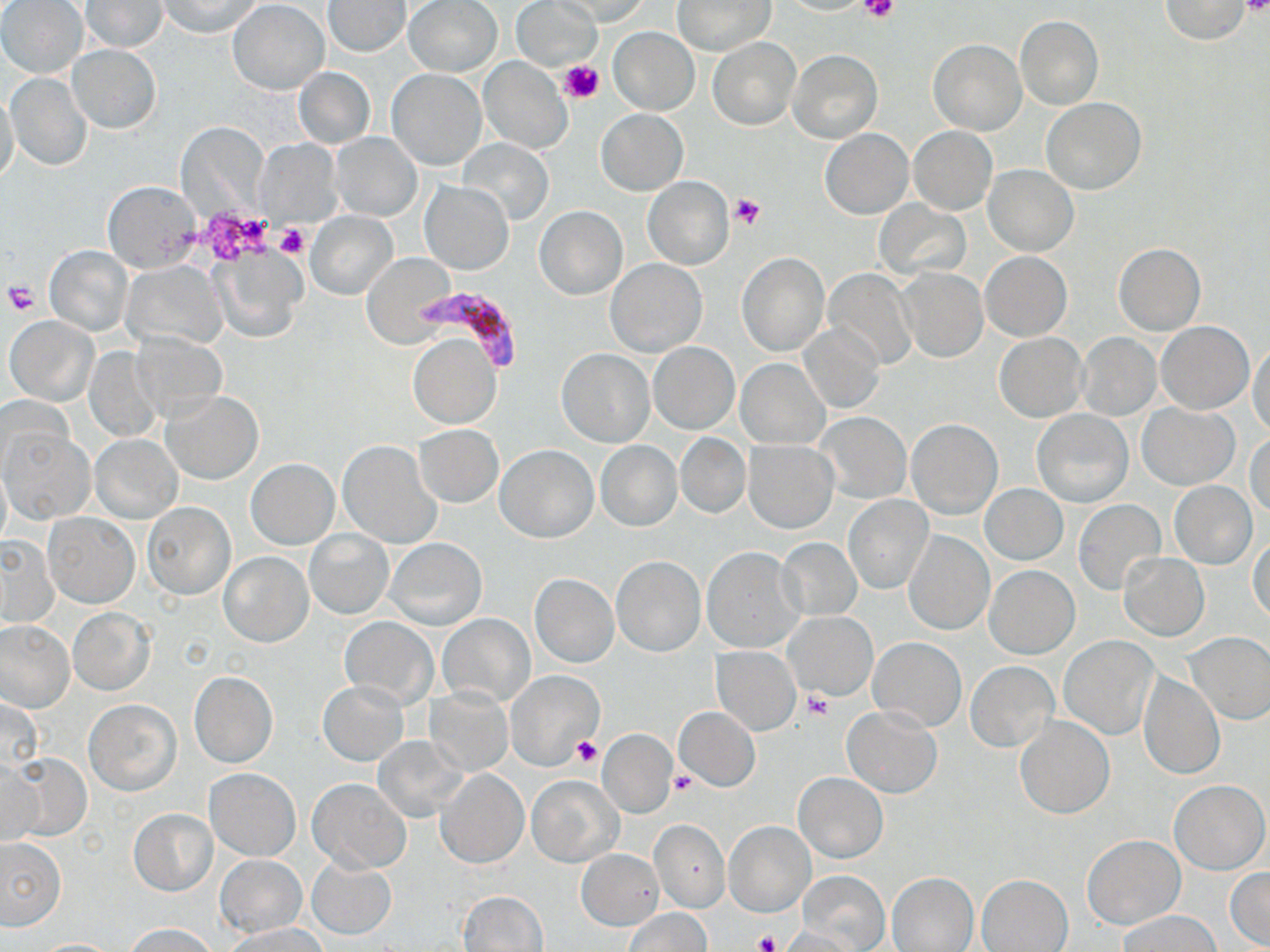

slide-level diagnosis = Plasmodium falciparum
preparation = thin blood smear
stain = May-Grünwald-Giemsa
image size = 1270×952 pixels
Plasmodium falciparum-infected red blood cell locations = approximate bounding boxes as (x1,y1)-(x2,y2) corner pairs in pixels: (421,286)-(524,368)
uninfected red blood cell locations = approximate bounding boxes as (x1,y1)-(x2,y2) corner pairs in pixels: (0,0)-(88,79), (158,0)-(262,37), (403,0)-(502,76), (552,0)-(653,25), (672,0)-(773,55), (1160,0)-(1251,43), (80,1)-(167,52), (228,1)-(329,94), (325,1)-(410,56), (511,1)-(603,73), (1015,16)-(1102,109), (609,26)-(700,114), (708,38)-(801,130), (929,39)-(1025,135), (67,45)-(160,133), (787,50)-(883,143), (479,57)-(573,154), (294,67)-(375,148), (387,68)-(486,170), (5,72)-(92,171), (0,93)-(20,187), (1041,98)-(1147,194), (596,110)-(687,194), (176,121)-(270,220), (909,127)-(998,215), (819,128)-(914,218), (330,133)-(422,220), (457,137)-(554,226), (253,140)-(338,222), (983,164)-(1079,255), (643,176)-(734,269), (103,180)-(201,272), (422,181)-(512,273), (875,200)-(971,280), (533,205)-(628,300), (305,211)-(397,299), (1113,243)-(1205,335), (44,245)-(133,336), (212,245)-(306,344), (981,251)-(1071,341), (361,253)-(454,347), (737,253)-(829,357), (606,258)-(706,357), (124,259)-(228,351), (896,268)-(987,362), (823,269)-(917,370), (5,316)-(99,406), (1155,321)-(1254,414), (800,322)-(884,414), (130,331)-(230,422), (994,333)-(1087,421), (408,334)-(501,429), (1077,334)-(1160,420), (1249,341)-(1270,437), (649,343)-(739,434), (83,345)-(164,442), (557,348)-(654,447), (736,358)-(829,448), (162,392)-(263,484), (0,395)-(73,478), (1138,403)-(1239,489), (1032,409)-(1134,508), (816,412)-(910,504), (906,419)-(1003,520), (415,425)-(503,507), (3,429)-(93,522), (1248,429)-(1270,520), (89,434)-(182,524), (675,434)-(749,517), (337,440)-(441,549), (595,440)-(682,532), (743,441)-(838,534), (495,445)-(598,542), (247,459)-(338,549), (0,462)-(10,551), (1170,482)-(1257,569), (979,484)-(1068,564), (843,495)-(933,595), (1074,499)-(1166,596), (141,502)-(236,599), (43,514)-(139,608), (305,529)-(393,619), (903,531)-(994,636), (0,535)-(60,627), (1249,536)-(1270,623), (386,538)-(487,630), (775,538)-(862,622), (702,548)-(802,652), (219,552)-(312,646), (1119,553)-(1209,641), (611,556)-(706,657), (984,564)-(1080,659), (530,574)-(618,668), (69,608)-(154,695), (786,612)-(876,699), (438,614)-(534,707), (338,617)-(438,707), (0,621)-(74,713), (1186,632)-(1270,725), (1059,636)-(1158,740), (869,638)-(966,732), (711,647)-(800,736), (965,661)-(1058,751), (190,670)-(278,767), (506,670)-(605,770), (1139,671)-(1224,779), (318,681)-(409,765), (426,688)-(513,774), (1,697)-(41,777), (84,700)-(181,795), (674,706)-(760,791), (842,706)-(941,797), (1015,715)-(1114,818), (597,728)-(676,816), (373,736)-(469,821), (9,752)-(90,844), (0,757)-(40,845), (203,768)-(300,860), (437,768)-(528,868), (793,771)-(889,862), (527,775)-(623,866), (307,778)-(411,872), (1170,780)-(1268,874), (129,808)-(218,896), (649,818)-(729,913), (724,821)-(813,916), (1083,834)-(1183,928), (0,837)-(69,930), (576,849)-(664,929), (215,853)-(306,937), (307,860)-(396,939), (1226,868)-(1270,949), (797,869)-(890,951), (888,873)-(977,952), (977,874)-(1071,952), (456,890)-(548,952), (623,907)-(711,952), (1117,911)-(1222,952), (125,922)-(216,952), (227,924)-(325,952), (775,926)-(860,951), (31,938)-(124,951)
field of view = single
modality = light microscopy
platelet locations = approximate bounding boxes as (x1,y1)-(x2,y2) corner pairs in pixels: (862,0)-(898,24), (1238,0)-(1269,17), (558,60)-(604,105), (729,193)-(767,231), (202,211)-(273,263), (276,223)-(309,258), (3,281)-(38,314), (805,692)-(833,720), (572,736)-(603,767), (669,769)-(698,794), (750,930)-(781,952)
magnification = 1000x